Locate every Plasmodium malariae-infected red blood cell.
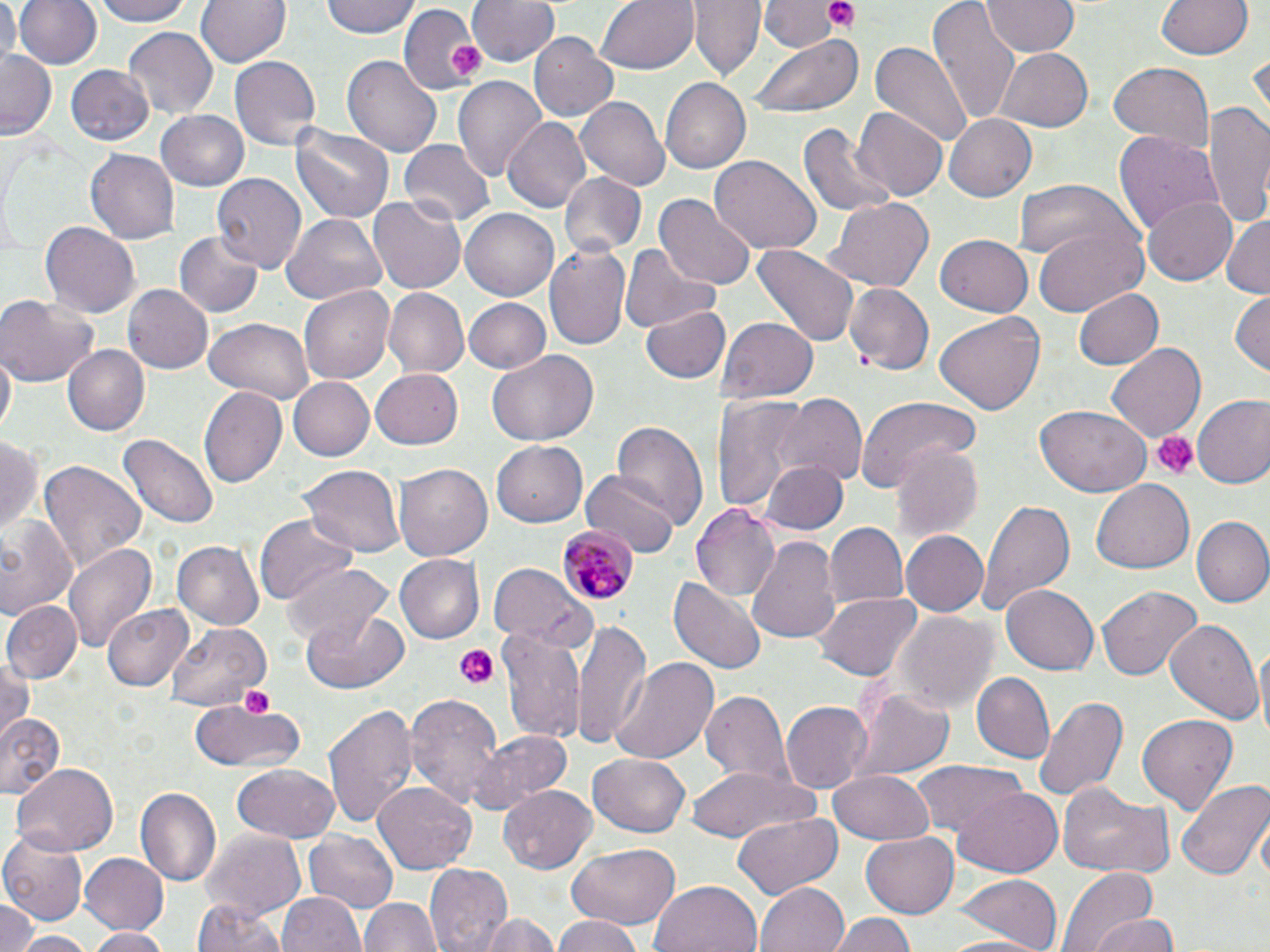

Approximate bounding boxes as named x1/y1/x2/y2 corners in pixels.
Plasmodium malariae-infected red blood cells: (x1=556, y1=525, x2=640, y2=608).

Summary:
  - Uninfected red blood cell locations: (x1=0, y1=0, x2=19, y2=69), (x1=13, y1=0, x2=102, y2=71), (x1=95, y1=0, x2=191, y2=26), (x1=196, y1=0, x2=289, y2=68), (x1=323, y1=0, x2=420, y2=39), (x1=469, y1=0, x2=561, y2=68), (x1=595, y1=0, x2=699, y2=74), (x1=689, y1=0, x2=764, y2=80), (x1=764, y1=0, x2=834, y2=51), (x1=928, y1=0, x2=1020, y2=127), (x1=981, y1=0, x2=1081, y2=57), (x1=1154, y1=0, x2=1257, y2=61), (x1=403, y1=4, x2=483, y2=98), (x1=761, y1=10, x2=849, y2=93), (x1=122, y1=28, x2=217, y2=122), (x1=530, y1=32, x2=620, y2=122), (x1=751, y1=34, x2=862, y2=119), (x1=867, y1=39, x2=975, y2=152), (x1=991, y1=49, x2=1091, y2=132), (x1=3, y1=52, x2=58, y2=138), (x1=344, y1=53, x2=441, y2=161), (x1=230, y1=56, x2=320, y2=149), (x1=1108, y1=62, x2=1214, y2=153), (x1=63, y1=65, x2=155, y2=148), (x1=453, y1=73, x2=547, y2=179), (x1=660, y1=77, x2=750, y2=172), (x1=576, y1=97, x2=669, y2=191), (x1=1205, y1=99, x2=1270, y2=230), (x1=854, y1=107, x2=946, y2=201), (x1=155, y1=109, x2=250, y2=190), (x1=944, y1=113, x2=1036, y2=201), (x1=504, y1=118, x2=592, y2=214), (x1=290, y1=121, x2=394, y2=225), (x1=802, y1=121, x2=896, y2=217), (x1=1114, y1=132, x2=1224, y2=238), (x1=400, y1=140, x2=494, y2=229), (x1=86, y1=148, x2=180, y2=244), (x1=710, y1=157, x2=821, y2=253), (x1=559, y1=170, x2=650, y2=259), (x1=212, y1=173, x2=306, y2=273), (x1=1012, y1=179, x2=1132, y2=265), (x1=657, y1=194, x2=755, y2=290), (x1=1143, y1=194, x2=1239, y2=285), (x1=367, y1=195, x2=465, y2=295), (x1=826, y1=197, x2=933, y2=294), (x1=459, y1=208, x2=559, y2=301), (x1=1222, y1=213, x2=1270, y2=298), (x1=281, y1=215, x2=387, y2=304), (x1=39, y1=219, x2=139, y2=314), (x1=1031, y1=222, x2=1145, y2=316), (x1=175, y1=231, x2=262, y2=317), (x1=934, y1=235, x2=1033, y2=316), (x1=545, y1=240, x2=633, y2=352), (x1=754, y1=242, x2=858, y2=350), (x1=621, y1=244, x2=722, y2=333), (x1=845, y1=283, x2=933, y2=373), (x1=121, y1=284, x2=213, y2=374), (x1=298, y1=285, x2=395, y2=386), (x1=1071, y1=287, x2=1163, y2=371), (x1=383, y1=289, x2=468, y2=377), (x1=1230, y1=289, x2=1269, y2=375), (x1=0, y1=292, x2=100, y2=386), (x1=464, y1=299, x2=549, y2=373), (x1=642, y1=301, x2=729, y2=384), (x1=934, y1=311, x2=1044, y2=418), (x1=204, y1=317, x2=315, y2=403), (x1=720, y1=317, x2=817, y2=403), (x1=1107, y1=343, x2=1206, y2=441), (x1=62, y1=344, x2=149, y2=436), (x1=2, y1=350, x2=15, y2=441), (x1=487, y1=352, x2=598, y2=446), (x1=370, y1=368, x2=463, y2=450), (x1=287, y1=376, x2=373, y2=462), (x1=199, y1=386, x2=287, y2=490), (x1=713, y1=392, x2=810, y2=513), (x1=775, y1=394, x2=866, y2=485), (x1=858, y1=395, x2=978, y2=494), (x1=1193, y1=397, x2=1270, y2=490), (x1=1036, y1=406, x2=1150, y2=497), (x1=612, y1=419, x2=709, y2=530), (x1=119, y1=433, x2=216, y2=528), (x1=0, y1=435, x2=44, y2=536), (x1=491, y1=439, x2=587, y2=529), (x1=890, y1=442, x2=982, y2=542), (x1=37, y1=461, x2=147, y2=576), (x1=394, y1=462, x2=495, y2=561), (x1=760, y1=462, x2=847, y2=534), (x1=300, y1=464, x2=406, y2=557), (x1=583, y1=469, x2=680, y2=561), (x1=1091, y1=480, x2=1194, y2=574), (x1=974, y1=500, x2=1073, y2=621), (x1=692, y1=502, x2=781, y2=604), (x1=255, y1=514, x2=356, y2=604), (x1=0, y1=517, x2=81, y2=619), (x1=1193, y1=517, x2=1270, y2=609), (x1=823, y1=523, x2=908, y2=608), (x1=901, y1=530, x2=989, y2=617), (x1=748, y1=536, x2=844, y2=646), (x1=63, y1=540, x2=156, y2=654), (x1=173, y1=541, x2=263, y2=628), (x1=393, y1=554, x2=483, y2=643), (x1=285, y1=562, x2=395, y2=647), (x1=489, y1=563, x2=593, y2=651), (x1=670, y1=575, x2=767, y2=674), (x1=1000, y1=585, x2=1097, y2=676), (x1=1097, y1=585, x2=1201, y2=681), (x1=816, y1=590, x2=920, y2=680), (x1=2, y1=600, x2=81, y2=684), (x1=102, y1=603, x2=193, y2=691), (x1=303, y1=610, x2=410, y2=693), (x1=892, y1=612, x2=995, y2=715), (x1=571, y1=616, x2=653, y2=752), (x1=1165, y1=616, x2=1263, y2=725), (x1=165, y1=619, x2=271, y2=712), (x1=498, y1=627, x2=587, y2=742), (x1=1254, y1=641, x2=1270, y2=742), (x1=0, y1=653, x2=34, y2=743), (x1=606, y1=656, x2=721, y2=767), (x1=972, y1=673, x2=1053, y2=762), (x1=851, y1=687, x2=953, y2=784), (x1=405, y1=689, x2=504, y2=807), (x1=699, y1=692, x2=793, y2=787), (x1=1032, y1=695, x2=1129, y2=803), (x1=191, y1=702, x2=305, y2=776), (x1=323, y1=702, x2=416, y2=832), (x1=782, y1=702, x2=870, y2=792), (x1=1135, y1=712, x2=1241, y2=814), (x1=0, y1=713, x2=65, y2=800), (x1=468, y1=731, x2=572, y2=815), (x1=586, y1=754, x2=692, y2=837), (x1=911, y1=759, x2=1025, y2=837), (x1=11, y1=763, x2=120, y2=856), (x1=232, y1=763, x2=341, y2=842), (x1=683, y1=765, x2=820, y2=841), (x1=829, y1=767, x2=933, y2=844), (x1=1176, y1=775, x2=1270, y2=882), (x1=373, y1=782, x2=476, y2=875), (x1=499, y1=784, x2=598, y2=871), (x1=1061, y1=785, x2=1172, y2=880), (x1=952, y1=786, x2=1063, y2=877), (x1=138, y1=787, x2=222, y2=889), (x1=733, y1=813, x2=843, y2=898), (x1=0, y1=827, x2=88, y2=923), (x1=200, y1=829, x2=307, y2=915), (x1=305, y1=831, x2=397, y2=911), (x1=861, y1=832, x2=959, y2=917), (x1=564, y1=842, x2=681, y2=932), (x1=78, y1=853, x2=167, y2=933), (x1=424, y1=862, x2=512, y2=952), (x1=1056, y1=867, x2=1159, y2=952), (x1=955, y1=875, x2=1061, y2=952), (x1=650, y1=879, x2=764, y2=952), (x1=755, y1=881, x2=849, y2=952), (x1=280, y1=892, x2=365, y2=952), (x1=361, y1=896, x2=441, y2=952), (x1=193, y1=898, x2=287, y2=952), (x1=0, y1=900, x2=38, y2=952), (x1=479, y1=912, x2=560, y2=952), (x1=831, y1=914, x2=919, y2=952), (x1=1089, y1=914, x2=1180, y2=952), (x1=549, y1=916, x2=648, y2=952), (x1=86, y1=926, x2=170, y2=952), (x1=11, y1=931, x2=97, y2=952), (x1=938, y1=933, x2=1051, y2=951)
  - Platelet locations: (x1=825, y1=1, x2=859, y2=32), (x1=445, y1=41, x2=485, y2=78), (x1=1150, y1=431, x2=1197, y2=480), (x1=451, y1=645, x2=500, y2=689), (x1=240, y1=684, x2=277, y2=715)
  - Slide-level diagnosis: Plasmodium malariae
  - Modality: optical microscopy
  - Image size: 1270×952 pixels
  - Stain: May-Grünwald-Giemsa
  - Preparation: thin blood smear
  - Magnification: 1000x
  - Field of view: one of a larger specimen